Assess this cell for malaria.
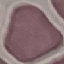

It is uninfected.

Cell patch, automatically extracted from a larger field of view and resized to 64 × 64 pixels. Thin blood smear. Photographed with a smartphone camera at the microscope eyepiece. Giemsa stain.